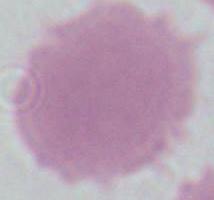

Summary:
  - Magnification: 1000x
  - Modality: micrograph
  - Identification: erythrocyte